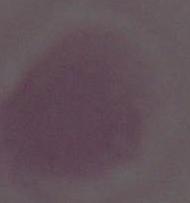
Summary:
  - Modality: photomicrograph
  - Identification: erythrocyte
  - Magnification: 1000x